Give the extent of all Plasmodium ovale-infected red blood cells.
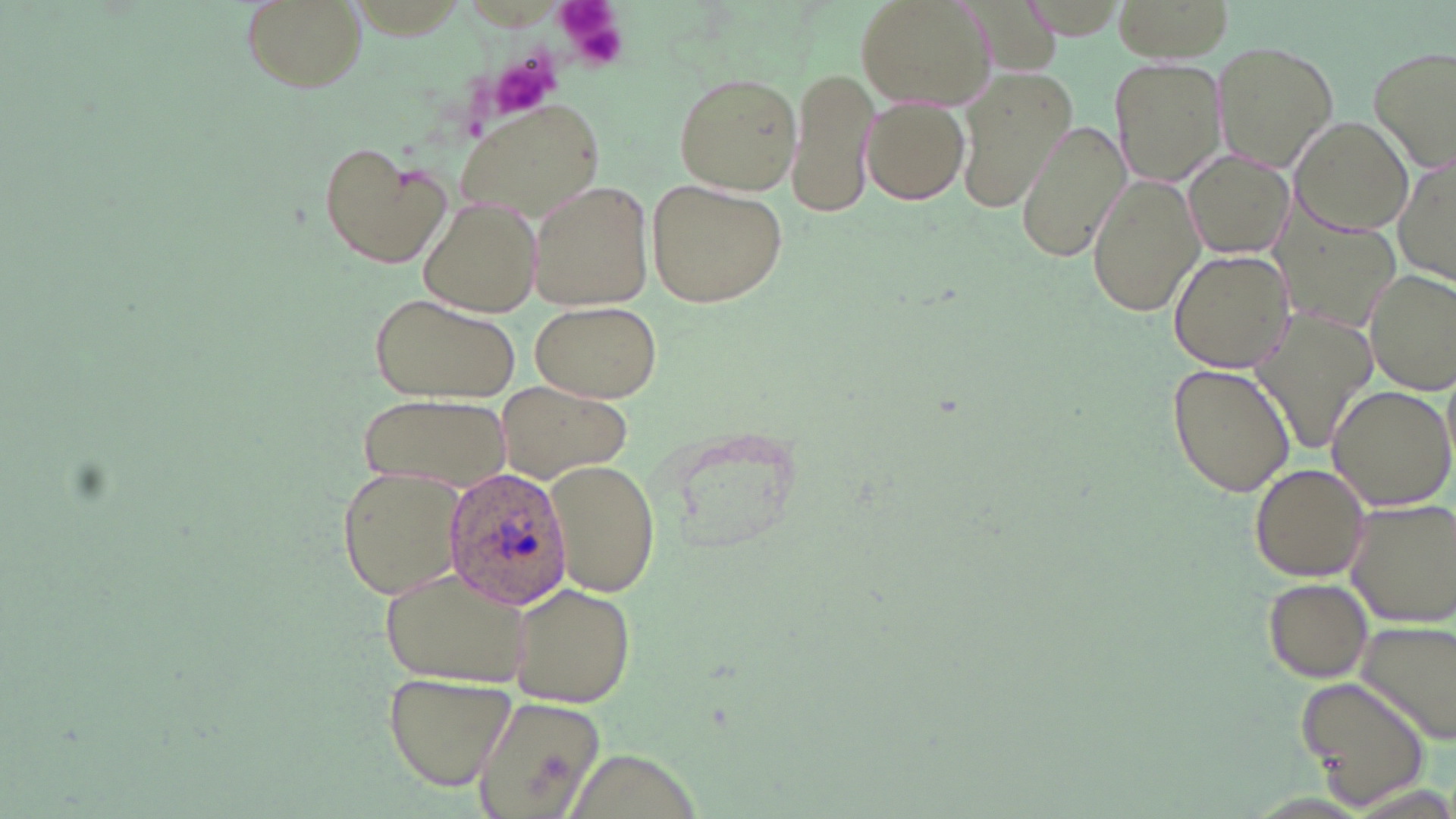
Approximate bounding boxes as (x1, y1, x2, y2) in pixels.
Plasmodium ovale-infected red blood cells: (442, 464, 574, 611).

Uninfected red blood cell locations: (239, 0, 366, 95), (855, 0, 998, 113), (1015, 0, 1134, 42), (1114, 0, 1234, 64), (1210, 41, 1339, 175), (1369, 45, 1456, 167), (1110, 56, 1225, 186), (786, 63, 879, 221), (955, 70, 1076, 216), (671, 71, 802, 195), (860, 96, 971, 207), (456, 99, 606, 223), (1017, 118, 1130, 264), (1292, 119, 1415, 237), (319, 142, 448, 266), (1394, 148, 1454, 292), (1183, 151, 1293, 257), (1086, 172, 1205, 320), (526, 177, 655, 313), (646, 177, 788, 309), (418, 195, 542, 318), (1276, 209, 1402, 332), (1168, 248, 1295, 373), (1364, 268, 1456, 394), (369, 290, 520, 403), (530, 300, 661, 403), (1251, 307, 1378, 454), (1168, 362, 1295, 499), (1326, 384, 1456, 511), (496, 385, 628, 480), (357, 394, 507, 491), (545, 462, 659, 595), (1249, 462, 1374, 583), (338, 464, 468, 600), (1343, 499, 1456, 628), (378, 567, 537, 687), (1261, 577, 1373, 682), (507, 583, 636, 706), (1355, 617, 1456, 745), (383, 671, 517, 790), (1296, 673, 1432, 809), (470, 695, 608, 819). Platelet locations: (555, 0, 629, 70), (494, 55, 558, 121). Slide-level diagnosis: Plasmodium ovale. Optical microscopy. One field of a larger specimen. May-Grünwald-Giemsa stain. Thin blood smear. Image is 1456×819 pixels. 1000x magnification.